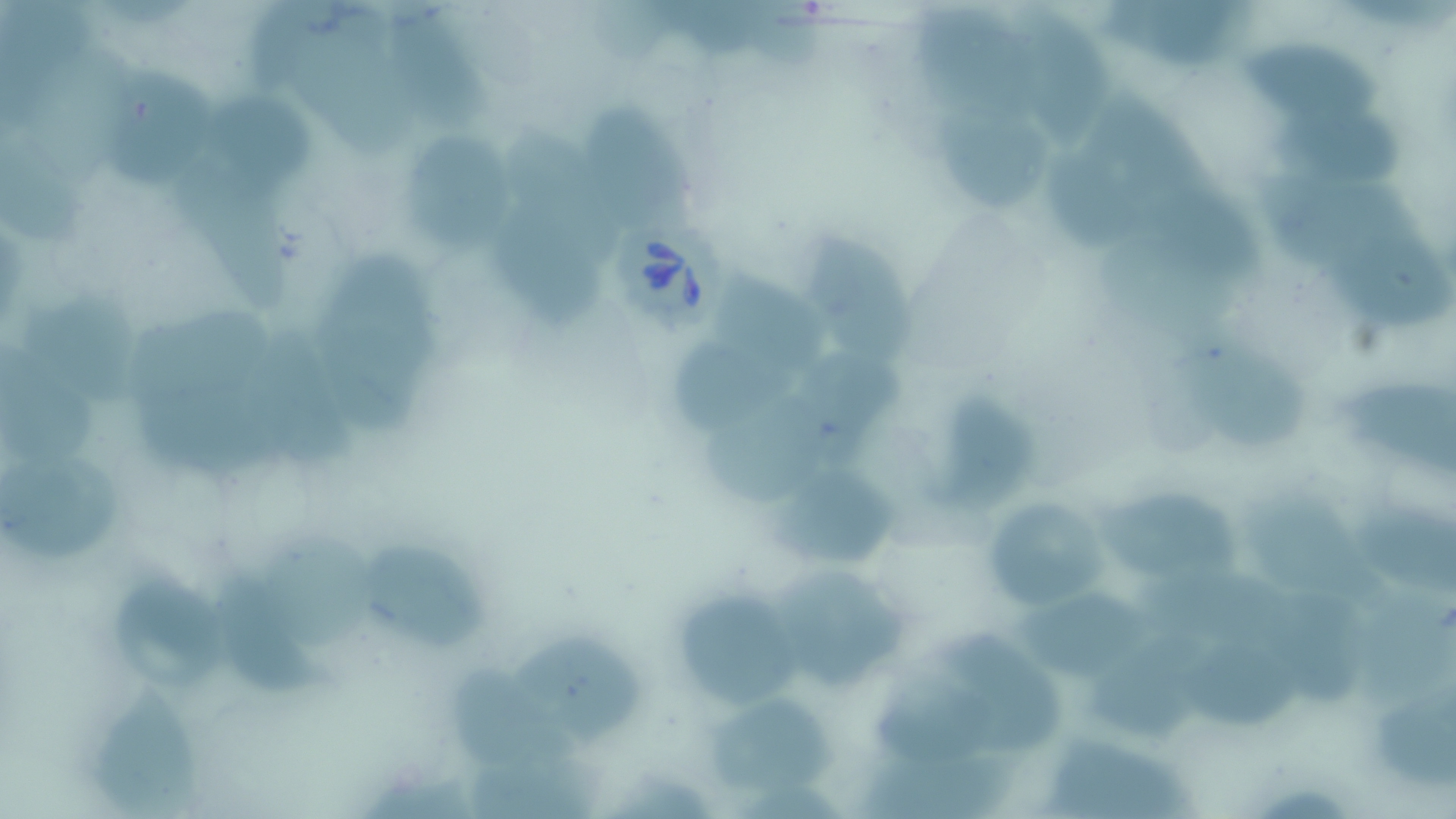

slide-level diagnosis = Babesia divergens
image size = 1456×819 pixels
magnification = 1000x
Babesia divergens-infected red blood cell locations = approximate bounding boxes as (x1, y1, x2, y2) in pixels: (606, 207, 733, 330)
modality = optical microscopy
stain = May-Grünwald-Giemsa
uninfected red blood cell locations = approximate bounding boxes as (x1, y1, x2, y2) in pixels: (251, 0, 349, 92), (385, 0, 495, 130), (1020, 0, 1118, 141), (1101, 0, 1247, 74), (912, 5, 1038, 116), (1226, 24, 1392, 128), (297, 29, 412, 160), (32, 45, 132, 187), (106, 62, 218, 192), (209, 83, 324, 193), (938, 87, 1052, 223), (1265, 89, 1408, 192), (1081, 95, 1219, 200), (574, 104, 715, 238), (507, 122, 618, 260), (407, 124, 525, 260), (0, 127, 88, 250), (1042, 142, 1133, 251), (171, 160, 290, 316), (1251, 171, 1433, 279), (1127, 179, 1269, 287), (503, 207, 606, 337), (802, 220, 920, 371), (1098, 232, 1241, 337), (1326, 238, 1455, 329), (311, 249, 439, 396), (716, 269, 840, 383), (19, 281, 139, 409), (129, 309, 278, 407), (247, 324, 359, 476), (1179, 330, 1304, 459), (668, 337, 799, 438), (0, 343, 106, 465), (803, 348, 918, 450), (1338, 359, 1456, 480), (137, 381, 301, 484), (703, 389, 833, 509), (951, 393, 1038, 514), (0, 452, 128, 562), (778, 456, 898, 573), (1099, 478, 1244, 594), (1243, 488, 1390, 611), (980, 494, 1112, 617), (1357, 508, 1456, 593), (261, 530, 384, 654), (358, 538, 489, 646), (772, 559, 915, 697), (210, 563, 326, 693), (1135, 566, 1293, 664), (112, 567, 233, 699), (677, 582, 809, 708), (1017, 584, 1173, 685), (1363, 592, 1456, 704), (1278, 595, 1374, 709), (514, 622, 650, 747), (933, 629, 1062, 750), (1089, 632, 1219, 740), (1183, 643, 1305, 734), (454, 668, 590, 766), (877, 675, 1005, 771), (1377, 676, 1456, 782), (88, 686, 210, 814), (705, 698, 844, 798), (1046, 733, 1200, 819), (854, 751, 1019, 819), (469, 759, 610, 819)
preparation = thin blood film
field of view = one of a larger specimen